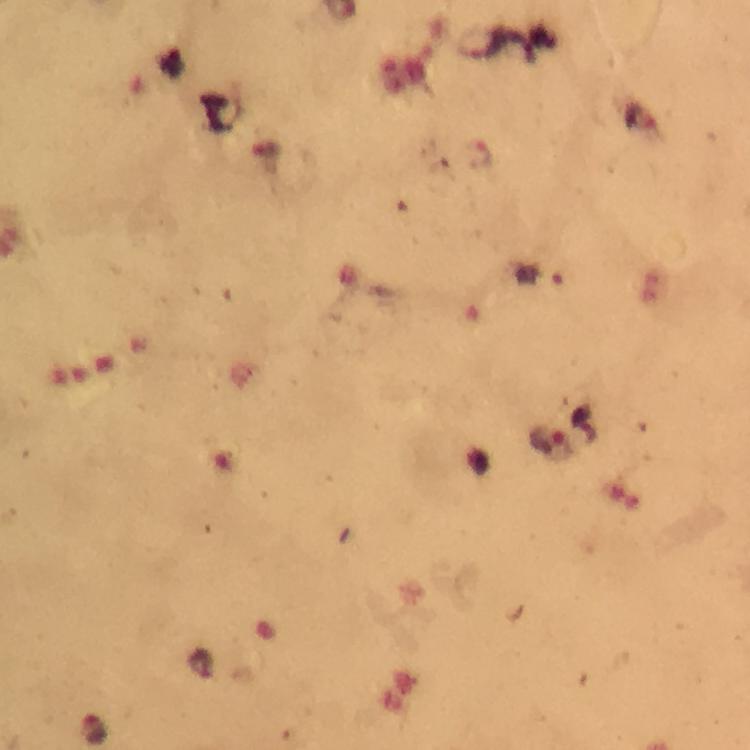
Approximate object centers, in pixels from the top-left corner.
Summary:
  - Plasmodium parasite locations: (x=548, y=439)
  - Immersion oil: used
  - Magnification: 100x
  - Preparation: thick smear
  - Capture: smartphone camera through the microscope
  - Stain: Giemsa
  - Cropped from: one field of view
  - Image size: 750×750 pixels
  - Context: from a diagnostic examination for malaria